State which parasite is depicted.
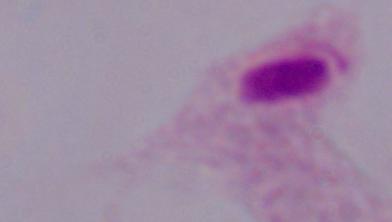

This is a trichomonad.

Summary:
  - Modality: micrograph
  - Magnification: 1000x